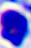
identification = leukocyte
modality = photomicrograph
magnification = 400x